Assess the morphology of the red blood cells.
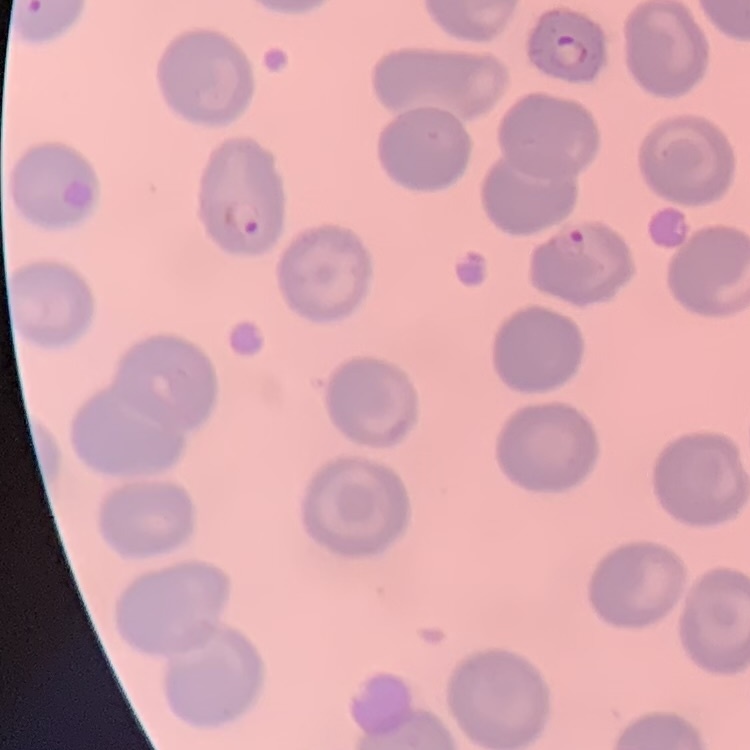
They show no rouleaux formation.

Summary:
  - Preparation: thin blood film
  - Image type: square crop of a larger photomicrograph
  - Stain: Field's or Giemsa